Outline platelets.
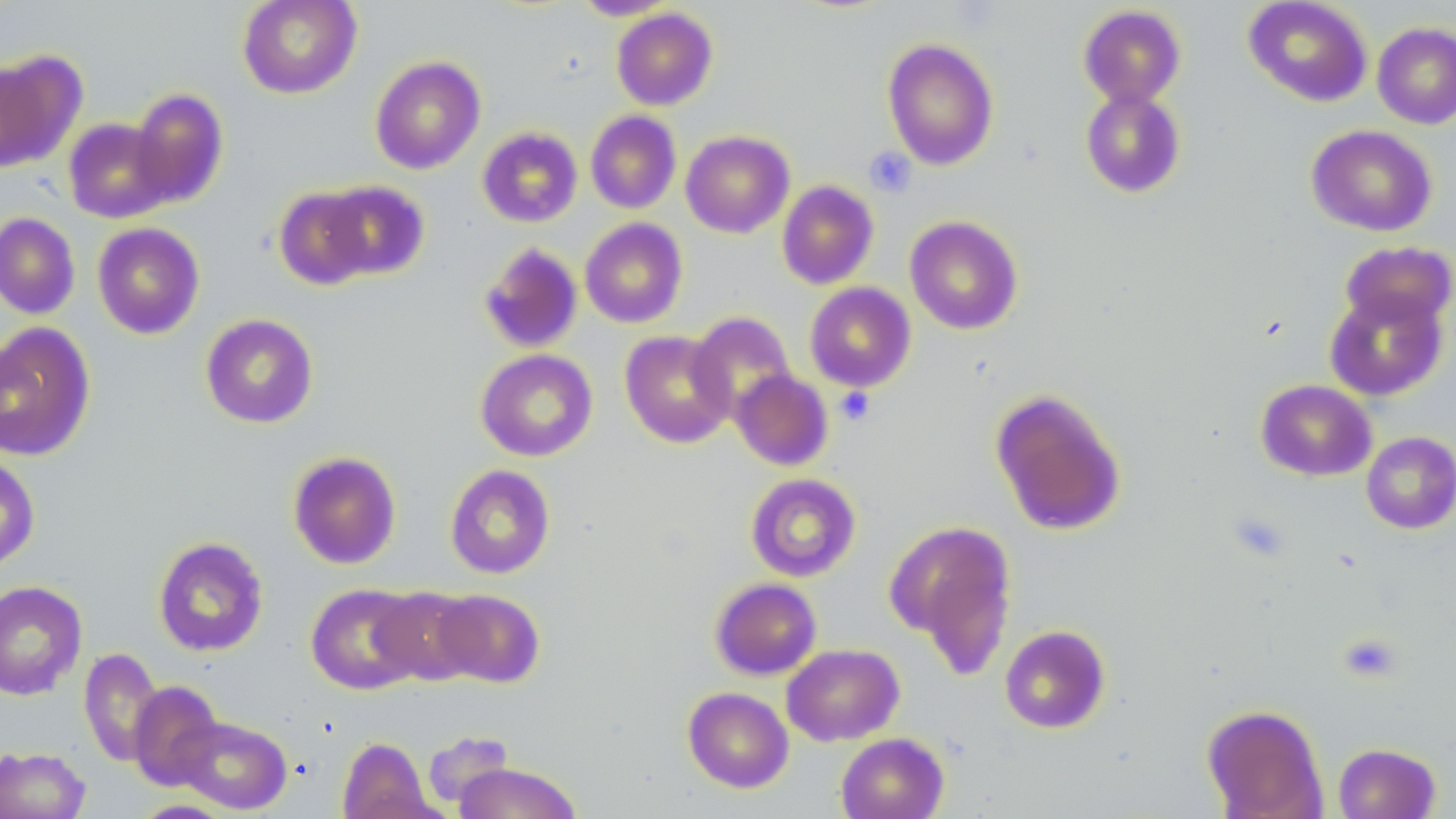
Approximate bounding boxes as (x1,y1)-(x2,y2) corner pairs in pixels.
Platelets: (864,146)-(916,197), (836,387)-(875,425).

Uninfected red blood cell locations: (237,0)-(362,99), (571,0)-(680,20), (1243,0)-(1373,107), (1078,4)-(1186,108), (611,7)-(718,110), (1372,22)-(1456,129), (882,38)-(999,170), (0,51)-(82,174), (369,55)-(486,174), (1079,87)-(1187,198), (129,88)-(229,207), (585,110)-(681,214), (63,118)-(173,223), (1306,124)-(1437,236), (477,126)-(583,227), (680,130)-(794,237), (321,180)-(430,280), (776,180)-(879,290), (273,186)-(377,290), (0,213)-(80,319), (904,215)-(1023,335), (580,217)-(688,328), (92,222)-(205,339), (1339,241)-(1456,332), (479,242)-(583,353), (804,282)-(917,392), (1324,287)-(1448,401), (687,311)-(797,421), (200,313)-(319,428), (0,322)-(96,460), (620,330)-(735,448), (475,349)-(598,461), (730,369)-(834,471), (1256,379)-(1377,481), (989,388)-(1127,536), (1361,431)-(1456,534), (287,451)-(401,569), (0,455)-(40,571), (445,464)-(556,579), (746,473)-(861,581), (885,519)-(1018,672), (152,536)-(269,657), (710,578)-(822,680), (0,579)-(87,700), (306,583)-(424,695), (371,586)-(480,685), (430,588)-(545,688), (999,625)-(1110,733), (782,643)-(904,746), (79,647)-(164,768), (128,681)-(224,791), (682,687)-(794,792), (1202,703)-(1328,818), (176,715)-(292,814), (422,729)-(515,809), (836,732)-(949,819), (337,736)-(436,819), (1332,742)-(1441,819), (0,746)-(91,819), (454,762)-(582,819), (130,800)-(236,818). Slide-level diagnosis: no evidence of blood parasites. Captured at 1000x magnification. Light microscopy. May-Grünwald-Giemsa stain. Image is 1456×819 pixels. Thin blood film. One field of a larger specimen.